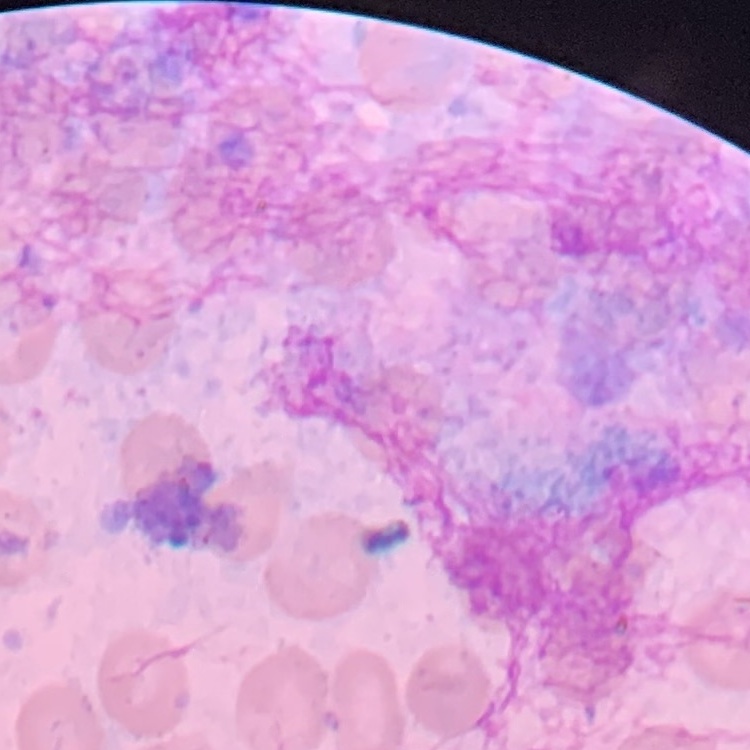

The erythrocytes show no rouleaux formation. Stained with either Field's or Giemsa. Thin blood smear. Square crop of a larger photomicrograph.